Give the extent of all uninfected red blood cells.
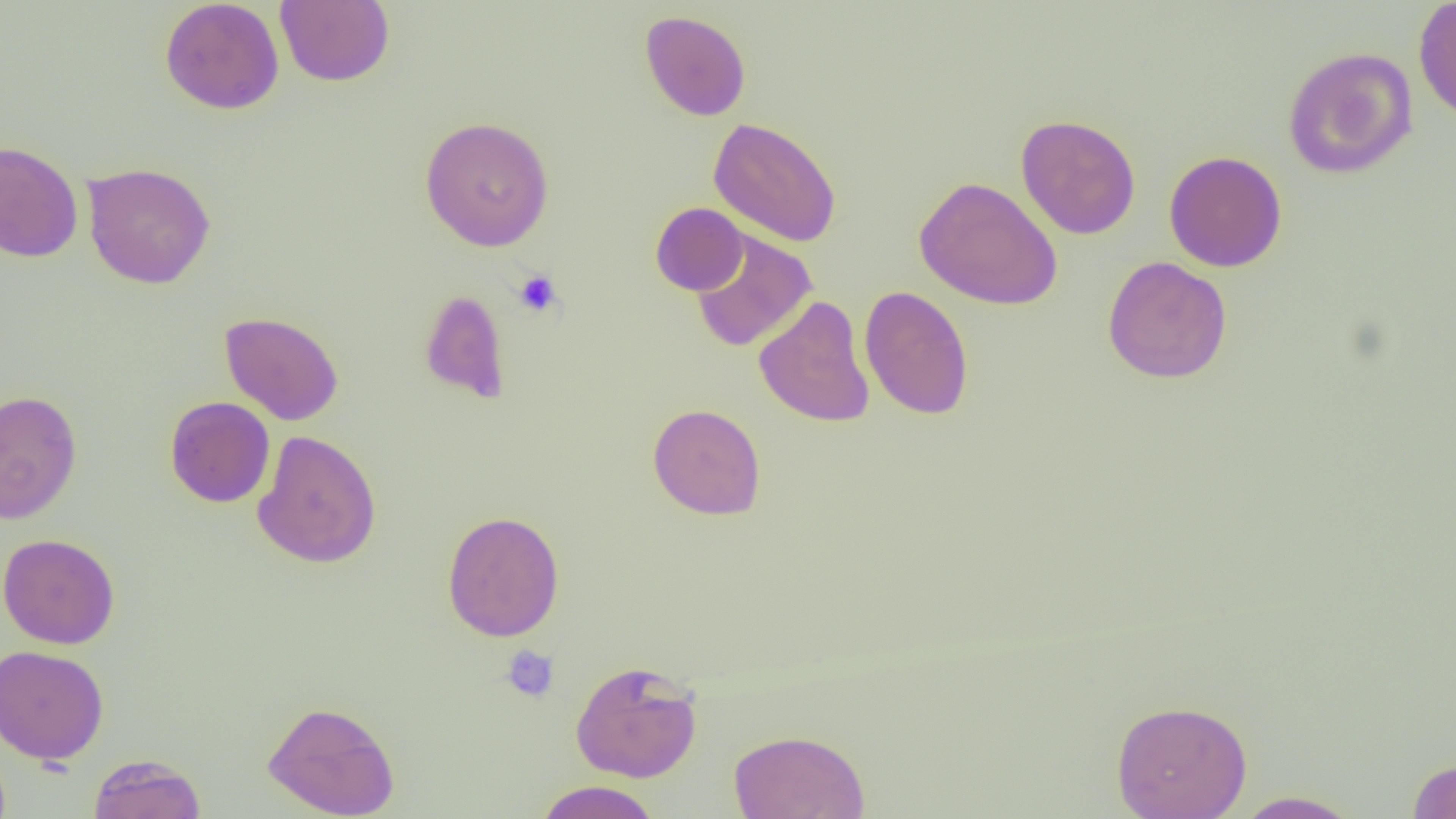
Approximate bounding boxes as named x1/y1/x2/y2 corners in pixels.
Uninfected red blood cells: (x1=159, y1=0, x2=284, y2=115), (x1=275, y1=0, x2=395, y2=87), (x1=1413, y1=0, x2=1456, y2=124), (x1=639, y1=10, x2=751, y2=121), (x1=1282, y1=46, x2=1418, y2=179), (x1=1015, y1=114, x2=1141, y2=239), (x1=419, y1=115, x2=555, y2=252), (x1=708, y1=117, x2=842, y2=247), (x1=0, y1=139, x2=83, y2=263), (x1=1164, y1=150, x2=1287, y2=272), (x1=82, y1=162, x2=216, y2=289), (x1=913, y1=176, x2=1063, y2=310), (x1=650, y1=202, x2=749, y2=296), (x1=689, y1=229, x2=817, y2=352), (x1=1102, y1=256, x2=1232, y2=384), (x1=860, y1=286, x2=974, y2=421), (x1=419, y1=289, x2=510, y2=404), (x1=754, y1=296, x2=875, y2=428), (x1=219, y1=311, x2=343, y2=426), (x1=0, y1=390, x2=83, y2=525), (x1=164, y1=396, x2=275, y2=508), (x1=647, y1=402, x2=766, y2=520), (x1=252, y1=429, x2=381, y2=569), (x1=441, y1=510, x2=565, y2=642), (x1=0, y1=533, x2=120, y2=649), (x1=0, y1=644, x2=109, y2=765), (x1=570, y1=660, x2=703, y2=783), (x1=1110, y1=698, x2=1252, y2=819), (x1=262, y1=700, x2=400, y2=818), (x1=728, y1=729, x2=871, y2=819), (x1=88, y1=753, x2=206, y2=819), (x1=1406, y1=757, x2=1456, y2=818), (x1=533, y1=780, x2=664, y2=819), (x1=1231, y1=790, x2=1364, y2=818).

Platelet locations: (x1=513, y1=269, x2=563, y2=317), (x1=500, y1=644, x2=560, y2=704). Slide-level diagnosis: negative for blood parasites. Captured at 1000x magnification. Thin blood film. Optical microscopy. Image is 1456×819 pixels. Single field of view.